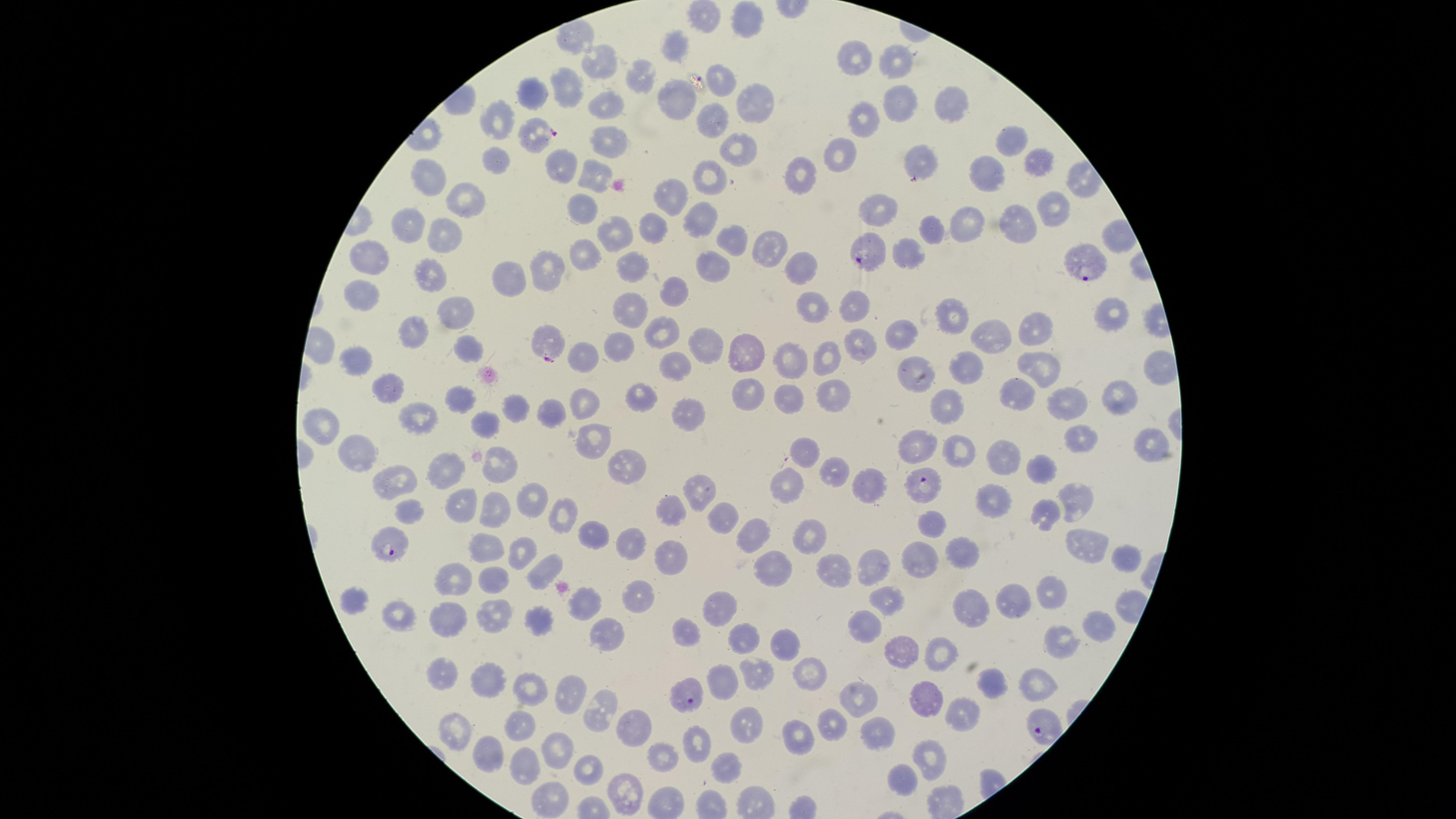

Approximate marker points as [x, y] in pixels.
Summary:
  - Parasitized red blood cells: [539, 135], [865, 252], [1078, 263], [544, 338], [921, 486], [392, 544], [686, 696], [1037, 724]
  - Uninfected red blood cells: [748, 21], [676, 48], [902, 62], [855, 63], [601, 65], [639, 77], [719, 79], [567, 94], [528, 99], [675, 99], [756, 101], [954, 104], [602, 107], [904, 107], [713, 120], [499, 121], [863, 123], [1010, 138], [604, 142], [737, 151], [841, 156], [1040, 158], [493, 159], [561, 163], [920, 164], [800, 172], [985, 175], [593, 177], [712, 179], [433, 180], [671, 195], [459, 205], [585, 205], [877, 206], [1055, 207], [701, 217], [970, 220], [1022, 220], [409, 222], [936, 227], [650, 235], [617, 237], [442, 238], [730, 242], [770, 243], [584, 246], [911, 246], [373, 256], [634, 262], [801, 268], [549, 269], [713, 270], [427, 275], [510, 279], [359, 292], [672, 296], [856, 305], [819, 306], [630, 309], [449, 311], [958, 313], [1111, 315], [1041, 325], [413, 326], [662, 328], [900, 332], [990, 334], [863, 343], [463, 347], [704, 347], [621, 351], [741, 351], [824, 351], [789, 357], [355, 359], [584, 360], [1037, 363], [673, 365], [967, 366], [1157, 366], [917, 369], [741, 386], [834, 386], [386, 387], [1018, 388], [637, 389], [1117, 392], [782, 394], [457, 400], [582, 404], [942, 404], [515, 406], [1067, 407], [678, 413], [550, 414], [421, 415], [483, 420], [325, 425], [1075, 438], [1150, 441], [592, 444], [920, 444], [808, 451], [960, 451], [362, 456], [1000, 458], [497, 464], [624, 467], [831, 470], [442, 472], [1044, 473], [393, 487], [782, 487], [870, 487], [695, 493], [492, 499], [991, 499], [1073, 499], [536, 500], [408, 504], [461, 510], [1046, 511], [560, 512], [672, 513], [721, 516], [936, 522], [593, 527], [749, 536], [807, 539], [627, 542], [488, 546], [1081, 546], [518, 549], [673, 554], [960, 556], [916, 557], [1123, 560], [877, 568], [541, 569], [775, 570], [836, 572], [494, 579], [451, 581], [1051, 593], [639, 602], [888, 603], [352, 605], [1012, 605], [967, 607], [720, 608], [400, 613], [490, 613], [581, 613], [535, 618], [868, 618], [1096, 621], [440, 623], [679, 632], [601, 634], [1060, 639], [741, 640], [780, 645], [902, 650], [939, 654], [813, 673], [442, 675], [755, 675], [720, 679], [485, 682], [1040, 682], [993, 684], [529, 691], [563, 696], [927, 698], [860, 703], [593, 716], [960, 717], [832, 724], [740, 725], [457, 727], [517, 729], [635, 729], [799, 733], [880, 735], [695, 742], [558, 749], [483, 754], [932, 758], [664, 759], [592, 763], [723, 767], [520, 770], [904, 783], [619, 785], [545, 793]
  - Capture: smartphone photograph through the microscope eyepiece
  - Stain: Giemsa
  - Species: Plasmodium falciparum
  - Presence: malaria parasites identified
  - Preparation: thin blood smear
  - Visible region: circular
  - Image size: 1456×819 pixels
  - Field of view: single